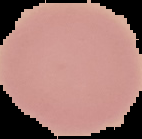
{
  "preparation": "thin blood smear",
  "result": "negative for malaria parasites",
  "image_size": "142×139 pixels",
  "image_type": "cell region segmented out of the field of view; surrounding area masked to black"
}